Report the malaria status of this cell.
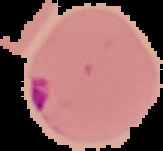
Parasitized.

From a thin blood film. The area outside the segmented cell region is set to black. Image is 163×151 pixels.